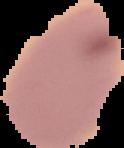

{
  "image_size": "124×148 pixels",
  "preparation": "thin blood film",
  "result": "no malaria parasites detected",
  "image_type": "cell region segmented out of the field of view; surrounding area masked to black"
}